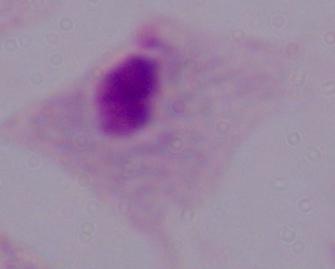

{
  "magnification": "1000x",
  "identification": "trichomonad",
  "modality": "micrograph"
}